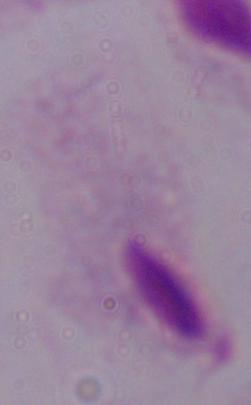 Micrograph. A trichomonad is seen. Captured at 1000x magnification.